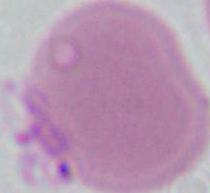
Summary:
  - Modality: micrograph
  - Identification: erythrocyte
  - Magnification: 1000x